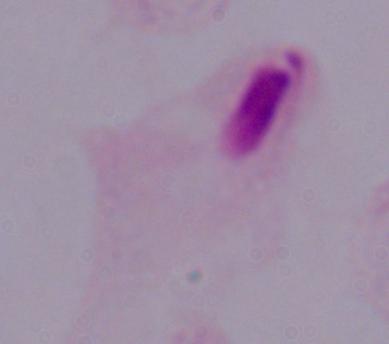
identification: trichomonad
modality: micrograph
magnification: 1000x